Point out each Plasmodium parasite.
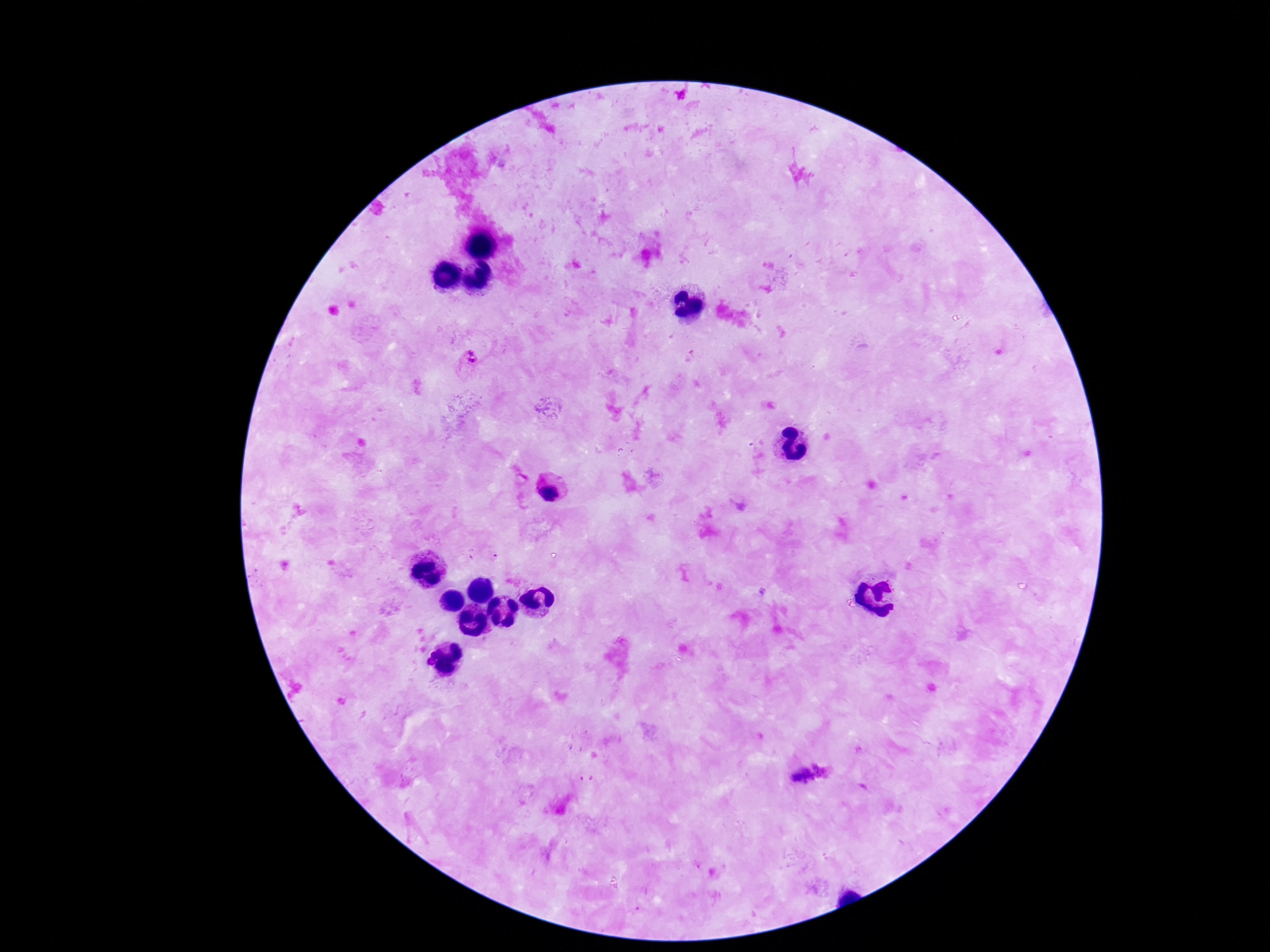
Approximate centers as {x, y} in pixels.
Plasmodium parasites: {470, 356}, {549, 491}, {823, 767}, {801, 776}.

capture = smartphone camera through the microscope eyepiece
magnification = 100x
preparation = thick peripheral-blood smear
patient malaria status = infected
stain = Giemsa
image size = 1270×952 pixels
field of view = single